Locate every P. falciparum parasite and give its life-cycle stage, and locate every leukocyte and any debris.
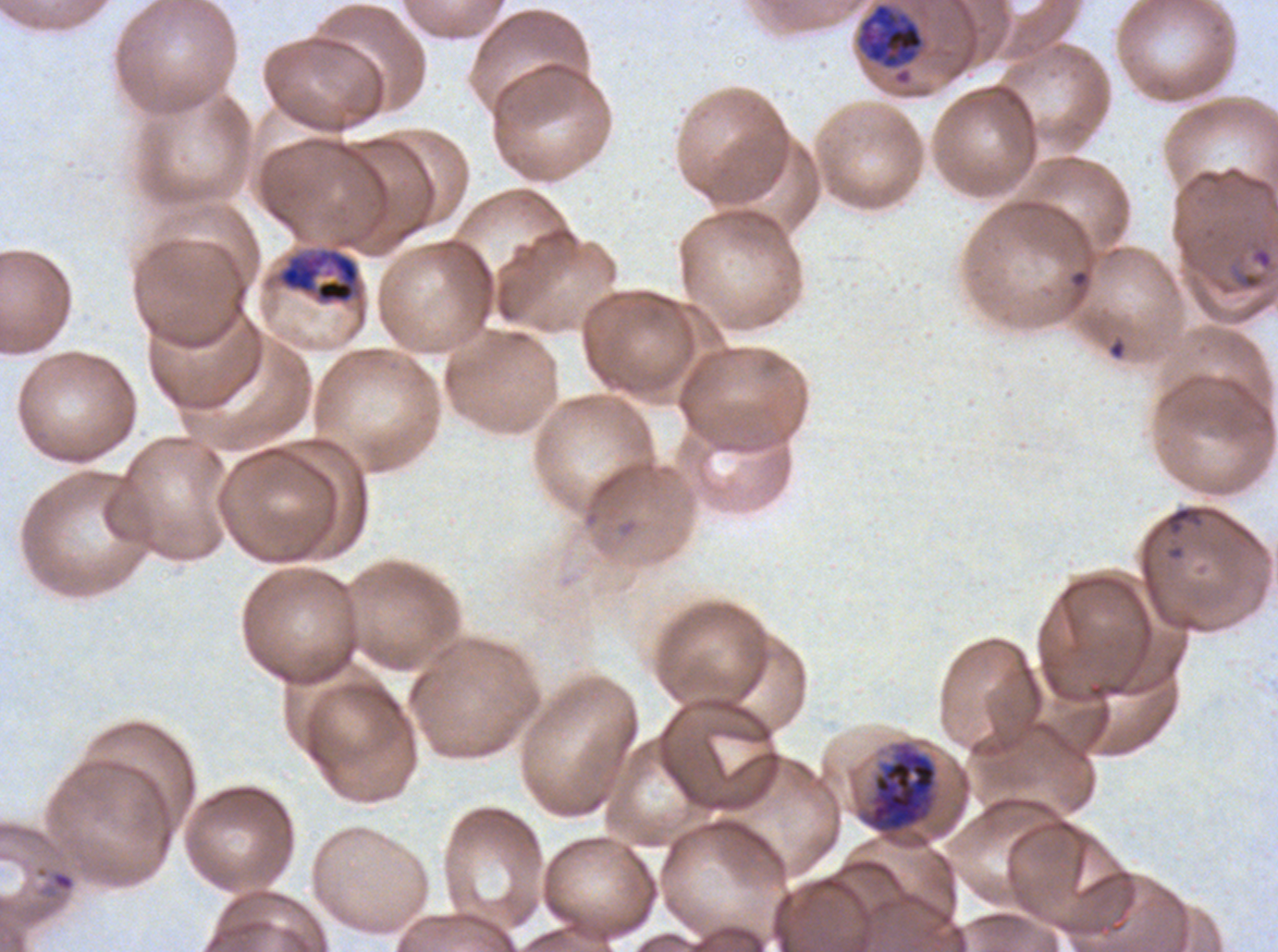

Approximate bounding boxes as (x1, y1, x2, y2) in pixels.
Rings: (1226, 261, 1267, 292), (1070, 269, 1090, 288), (42, 869, 76, 899).
Late trophozoites: (854, 1, 926, 86).
Early schizonts: (277, 248, 361, 304).
Late schizonts: (867, 744, 938, 833).
Debris: (1164, 506, 1202, 535).
No late-ring/early-trophozoite forms, mid trophozoites, segmenters, gametocytes, or leukocytes observed.

Image is 1278×952 pixels. Thin blood film. Giemsa-stained preparation. One sub-image of a larger composite. Ex-vivo P. falciparum culture from a patient in The Gambia, grown for 24 to 48 hours. Life-cycle stages observed: ring, late trophozoite, early schizont, late schizont.